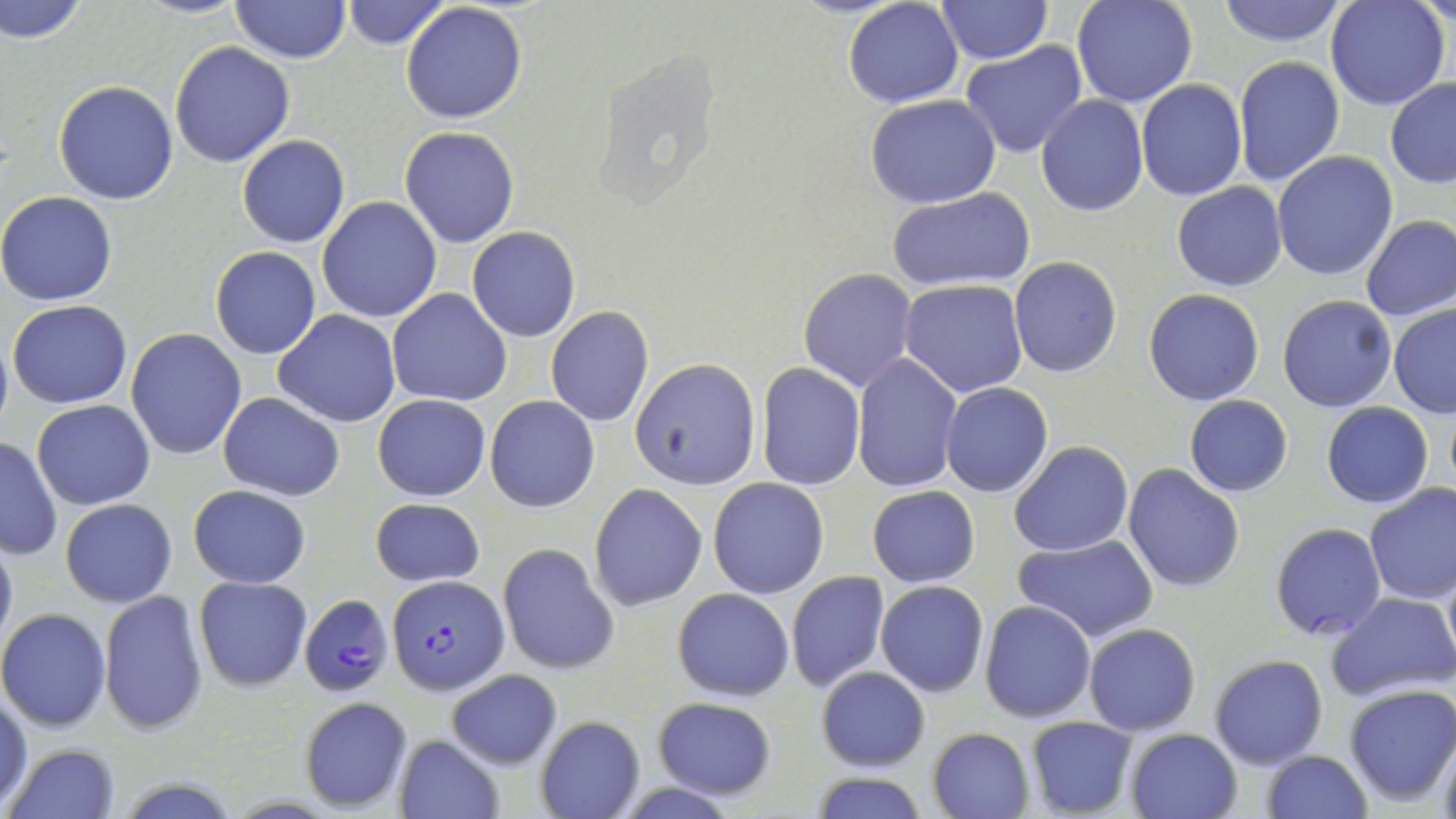
Approximate bounding boxes as (x1, y1, x2, y2) in pixels. Plasmodium falciparum-infected red blood cell locations: (387, 575, 506, 696), (301, 594, 390, 696). Uninfected red blood cell locations: (0, 0, 90, 46), (136, 0, 248, 20), (231, 0, 349, 64), (340, 0, 450, 49), (843, 0, 964, 109), (1072, 0, 1198, 107), (1214, 0, 1350, 48), (1325, 0, 1451, 111), (935, 1, 1052, 65), (401, 2, 528, 122), (959, 40, 1088, 158), (169, 42, 295, 168), (1234, 55, 1344, 185), (1385, 76, 1456, 188), (1136, 80, 1248, 201), (53, 81, 178, 204), (865, 94, 1002, 207), (1035, 94, 1148, 215), (400, 127, 520, 248), (236, 134, 350, 248), (1272, 151, 1397, 281), (1172, 182, 1287, 292), (886, 187, 1035, 293), (0, 191, 119, 307), (315, 196, 442, 322), (1360, 215, 1456, 323), (466, 227, 581, 342), (209, 247, 322, 360), (1009, 257, 1122, 376), (799, 268, 918, 391), (899, 278, 1028, 397), (386, 289, 511, 406), (1143, 289, 1265, 406), (1278, 295, 1398, 412), (8, 299, 133, 408), (1388, 304, 1456, 417), (545, 307, 655, 427), (273, 311, 402, 426), (0, 329, 13, 444), (126, 329, 246, 460), (852, 355, 962, 493), (631, 358, 760, 489), (755, 364, 865, 489), (941, 383, 1052, 497), (218, 393, 345, 500), (373, 394, 491, 502), (484, 395, 600, 513), (1183, 396, 1293, 497), (32, 400, 157, 510), (1322, 403, 1433, 508), (0, 436, 62, 560), (1010, 440, 1133, 557), (1123, 463, 1247, 592), (708, 477, 829, 599), (589, 482, 709, 612), (189, 484, 310, 588), (1363, 484, 1456, 604), (867, 485, 980, 587), (370, 497, 485, 588), (60, 499, 178, 607), (1270, 522, 1387, 641), (0, 527, 17, 658), (1011, 533, 1158, 642), (498, 544, 618, 676), (1440, 554, 1455, 675), (786, 572, 890, 692), (194, 575, 312, 691), (876, 581, 989, 698), (672, 587, 795, 703), (99, 590, 209, 736), (1328, 592, 1456, 700), (979, 601, 1096, 723), (0, 607, 113, 731), (1084, 624, 1201, 734), (1209, 655, 1328, 771), (816, 666, 930, 771), (446, 670, 562, 769), (1343, 685, 1456, 806), (1, 692, 32, 810), (299, 697, 414, 811), (650, 697, 777, 800), (535, 714, 645, 818), (1024, 716, 1137, 817), (1433, 727, 1456, 819), (929, 728, 1035, 818), (1126, 728, 1241, 818), (393, 734, 504, 818), (5, 743, 120, 818), (1263, 750, 1373, 819), (805, 771, 932, 819). Slide-level diagnosis: Plasmodium falciparum. Light microscopy. May-Grünwald-Giemsa-stained preparation. Thin blood smear. Single field of view. Captured at 1000x magnification. Image is 1456×819 pixels.